Classify this cell by malaria status.
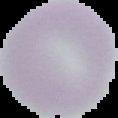
Uninfected.

preparation = thin blood film
image size = 118×118 pixels
image type = segmented cell region with the area outside set to black